Outline each uninfected red blood cell.
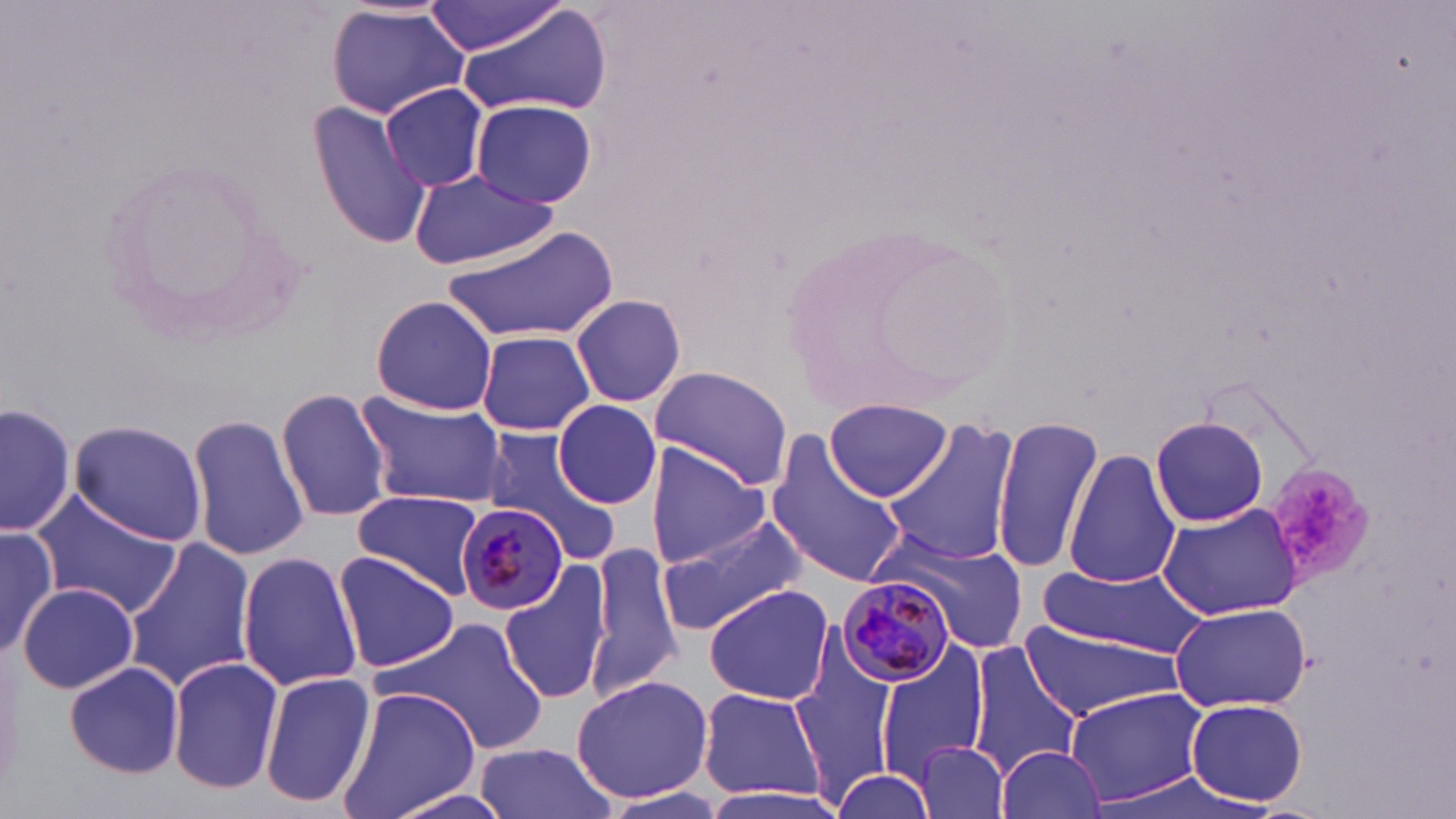
Approximate bounding boxes as (x1,y1)-(x2,y2) corner pairs in pixels.
Uninfected red blood cells: (421,1)-(569,55), (460,3)-(610,119), (326,7)-(471,118), (380,83)-(491,193), (470,99)-(597,207), (307,101)-(431,249), (404,168)-(557,269), (442,225)-(620,343), (571,293)-(688,406), (370,295)-(499,416), (477,330)-(594,436), (649,366)-(795,492), (278,386)-(396,523), (357,392)-(506,508), (825,398)-(953,498), (553,400)-(663,509), (1,401)-(75,539), (188,412)-(308,562), (1149,415)-(1267,525), (992,417)-(1098,568), (883,418)-(1020,567), (69,421)-(209,544), (480,432)-(618,560), (764,437)-(905,587), (648,444)-(771,565), (1063,450)-(1179,588), (352,489)-(484,595), (29,491)-(178,615), (1157,502)-(1305,621), (656,512)-(806,637), (0,526)-(56,659), (879,528)-(1029,656), (122,539)-(257,691), (586,543)-(682,698), (236,552)-(365,691), (334,553)-(459,672), (502,560)-(615,706), (1038,564)-(1209,655), (18,583)-(140,694), (703,583)-(836,706), (1170,603)-(1313,712), (380,616)-(554,759), (1019,624)-(1182,720), (963,644)-(1081,776), (876,649)-(988,778), (167,657)-(285,795), (65,660)-(187,778), (790,664)-(901,796), (260,671)-(375,808), (571,674)-(713,803), (1064,685)-(1208,808), (337,686)-(481,819), (696,687)-(830,802), (1184,698)-(1310,808), (913,740)-(1013,819), (470,741)-(615,819), (997,745)-(1108,819), (827,768)-(939,818), (692,782)-(853,819), (376,786)-(522,819).

slide-level diagnosis = Plasmodium malariae
modality = light microscopy
Plasmodium malariae-infected red blood cell locations = approximate bounding boxes as (x1,y1)-(x2,y2) corner pairs in pixels: (1266,459)-(1378,588), (459,503)-(571,616), (839,576)-(956,683)
stain = May-Grünwald-Giemsa
preparation = thin blood smear
magnification = 1000x
field of view = one of a larger specimen
image size = 1456×819 pixels